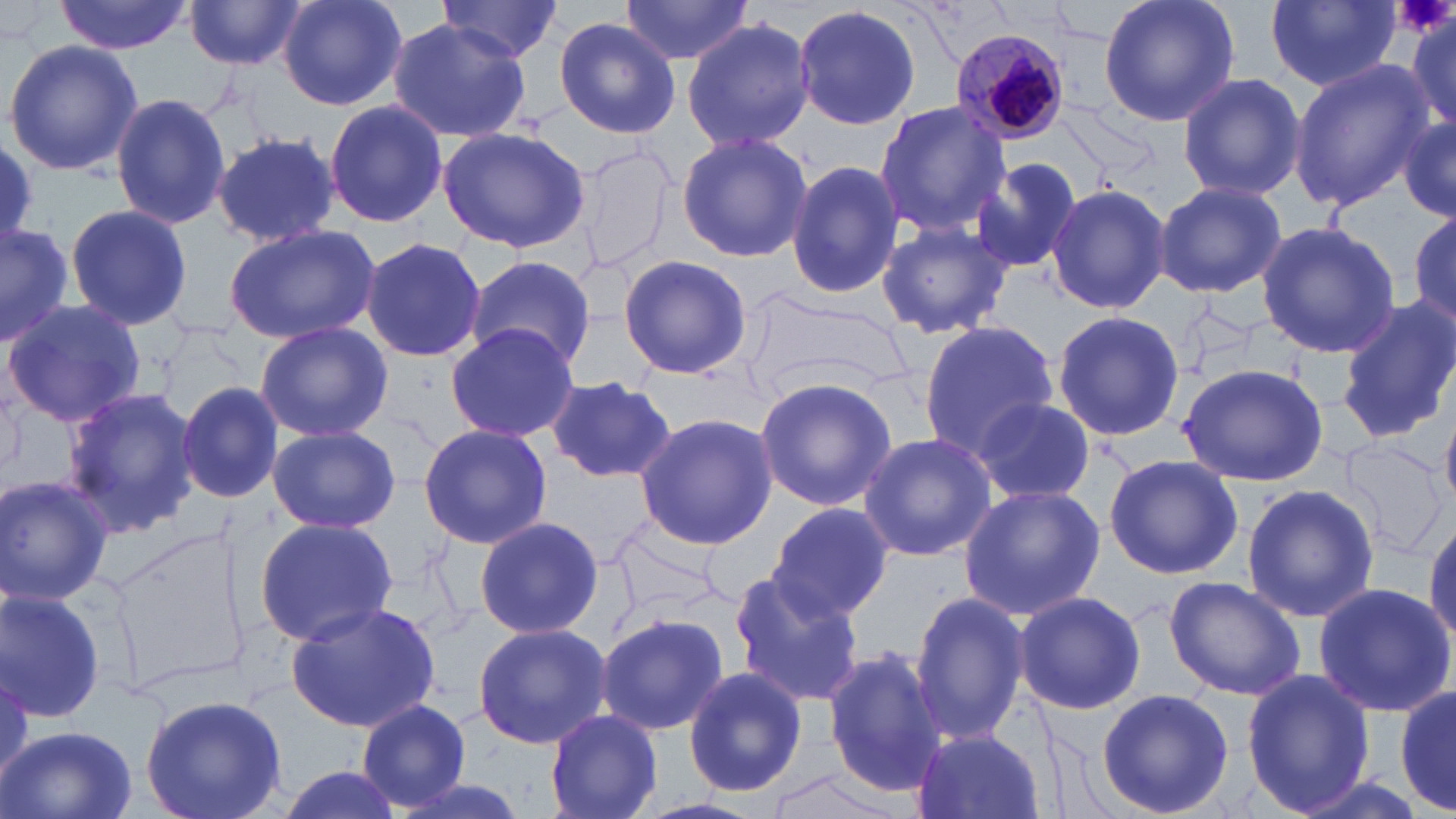

Summary:
  - Coordinate format: approximate bounding boxes as named x1/y1/x2/y2 corners in pixels
  - Uninfected red blood cell locations: (x1=55, y1=0, x2=190, y2=54), (x1=277, y1=0, x2=408, y2=111), (x1=618, y1=0, x2=755, y2=67), (x1=1096, y1=0, x2=1241, y2=130), (x1=186, y1=1, x2=305, y2=72), (x1=437, y1=1, x2=563, y2=64), (x1=1267, y1=1, x2=1402, y2=91), (x1=794, y1=3, x2=921, y2=133), (x1=1403, y1=8, x2=1455, y2=135), (x1=552, y1=16, x2=680, y2=138), (x1=682, y1=17, x2=813, y2=152), (x1=387, y1=20, x2=528, y2=143), (x1=2, y1=39, x2=145, y2=177), (x1=1288, y1=60, x2=1434, y2=212), (x1=1176, y1=71, x2=1306, y2=202), (x1=111, y1=93, x2=230, y2=229), (x1=324, y1=98, x2=447, y2=229), (x1=872, y1=98, x2=1011, y2=239), (x1=1397, y1=108, x2=1456, y2=228), (x1=437, y1=125, x2=593, y2=252), (x1=675, y1=131, x2=813, y2=263), (x1=209, y1=132, x2=341, y2=244), (x1=0, y1=140, x2=42, y2=244), (x1=972, y1=157, x2=1086, y2=277), (x1=785, y1=158, x2=903, y2=300), (x1=1154, y1=180, x2=1287, y2=299), (x1=1045, y1=182, x2=1171, y2=315), (x1=66, y1=203, x2=192, y2=331), (x1=1406, y1=207, x2=1456, y2=335), (x1=876, y1=218, x2=1012, y2=339), (x1=0, y1=220, x2=77, y2=343), (x1=1255, y1=221, x2=1400, y2=359), (x1=222, y1=224, x2=380, y2=346), (x1=362, y1=237, x2=485, y2=362), (x1=618, y1=254, x2=753, y2=382), (x1=466, y1=255, x2=595, y2=373), (x1=1336, y1=295, x2=1456, y2=444), (x1=2, y1=300, x2=147, y2=428), (x1=1052, y1=308, x2=1183, y2=443), (x1=918, y1=319, x2=1059, y2=458), (x1=253, y1=321, x2=392, y2=443), (x1=445, y1=323, x2=582, y2=442), (x1=1175, y1=362, x2=1329, y2=486), (x1=543, y1=372, x2=678, y2=483), (x1=754, y1=377, x2=897, y2=509), (x1=176, y1=379, x2=284, y2=502), (x1=61, y1=387, x2=199, y2=539), (x1=972, y1=398, x2=1096, y2=503), (x1=1442, y1=409, x2=1456, y2=510), (x1=633, y1=412, x2=779, y2=548), (x1=266, y1=424, x2=401, y2=532), (x1=417, y1=424, x2=552, y2=548), (x1=858, y1=432, x2=995, y2=562), (x1=1102, y1=453, x2=1245, y2=579), (x1=0, y1=474, x2=116, y2=607), (x1=1242, y1=483, x2=1381, y2=621), (x1=957, y1=485, x2=1105, y2=618), (x1=766, y1=502, x2=892, y2=624), (x1=1424, y1=513, x2=1456, y2=649), (x1=253, y1=516, x2=399, y2=646), (x1=473, y1=516, x2=604, y2=641), (x1=610, y1=523, x2=724, y2=625), (x1=731, y1=572, x2=868, y2=707), (x1=1164, y1=576, x2=1307, y2=701), (x1=1313, y1=583, x2=1455, y2=718), (x1=0, y1=586, x2=108, y2=723), (x1=908, y1=590, x2=1030, y2=745), (x1=1013, y1=590, x2=1146, y2=715), (x1=286, y1=600, x2=443, y2=734), (x1=595, y1=610, x2=730, y2=737), (x1=471, y1=621, x2=612, y2=750), (x1=823, y1=646, x2=949, y2=798), (x1=682, y1=665, x2=809, y2=796), (x1=1241, y1=668, x2=1376, y2=814), (x1=1392, y1=681, x2=1455, y2=816), (x1=1095, y1=686, x2=1235, y2=818), (x1=139, y1=693, x2=288, y2=819), (x1=356, y1=700, x2=474, y2=810), (x1=545, y1=708, x2=663, y2=818), (x1=3, y1=724, x2=137, y2=819), (x1=910, y1=727, x2=1044, y2=819), (x1=271, y1=765, x2=409, y2=819), (x1=754, y1=765, x2=907, y2=819), (x1=385, y1=775, x2=536, y2=819)
  - Plasmodium malariae-infected red blood cell locations: (x1=951, y1=28, x2=1070, y2=146)
  - Platelet locations: (x1=1402, y1=0, x2=1449, y2=37)
  - Slide-level diagnosis: Plasmodium malariae
  - Stain: May-Grünwald-Giemsa
  - Image size: 1456×819 pixels
  - Modality: optical microscopy
  - Magnification: 1000x
  - Preparation: thin blood smear
  - Field of view: one of a larger specimen